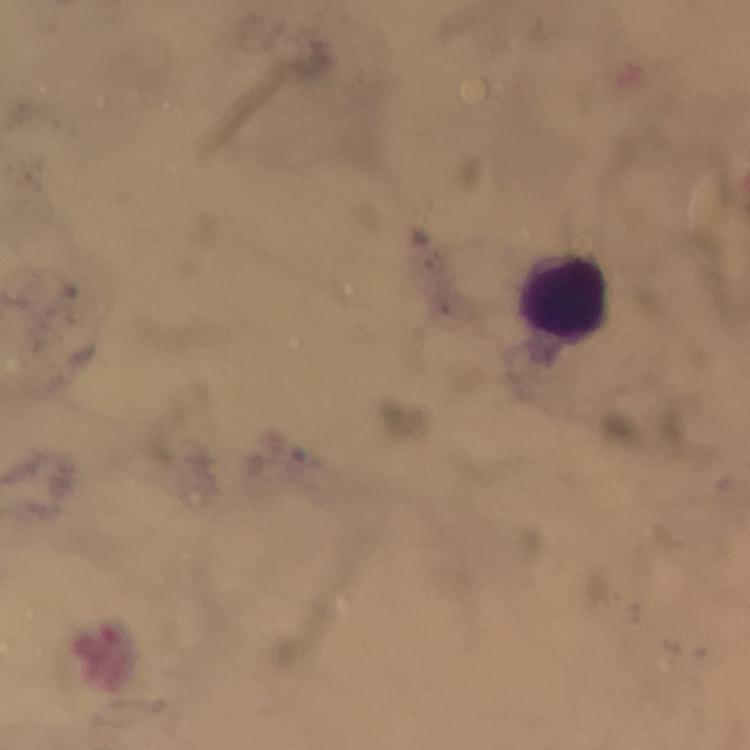

Approximate centers as {x, y} in pixels.
Summary:
  - Leukocyte locations: {566, 296}
  - Stain: Giemsa
  - Immersion oil: applied
  - Image size: 750×750 pixels
  - Magnification: 100x
  - Preparation: thick smear
  - Capture: smartphone camera through the microscope
  - Malaria parasites: none detected
  - Context: from a diagnostic examination for malaria
  - Cropped from: one field of view